Point out each malaria parasite.
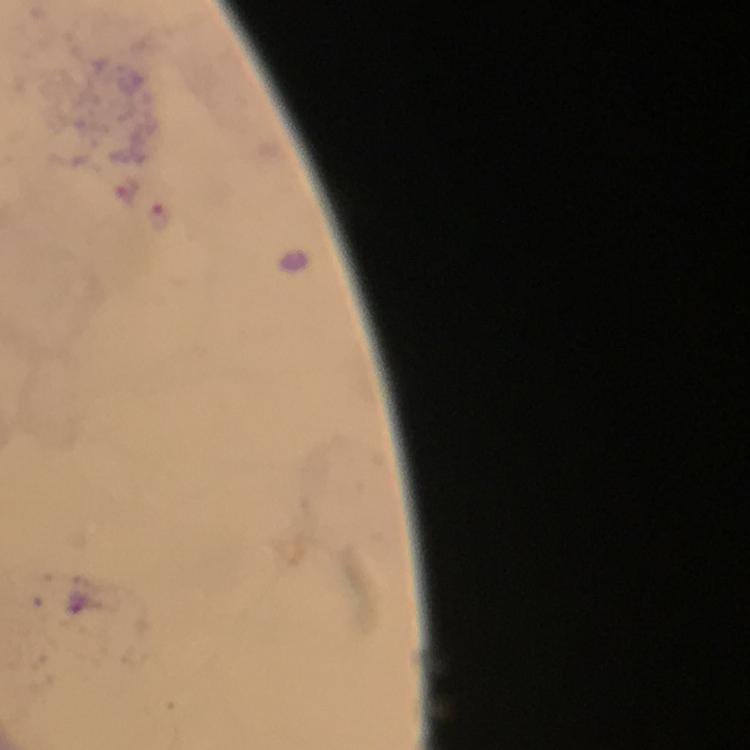

Approximate centers as {x, y} in pixels.
Malaria parasites: {129, 188}, {159, 216}.

capture = smartphone photograph through a microscope
image size = 750×750 pixels
preparation = thick blood film
context = from a diagnostic examination for malaria
immersion oil = used
magnification = 100x
stain = Giemsa
cropped from = one field of view